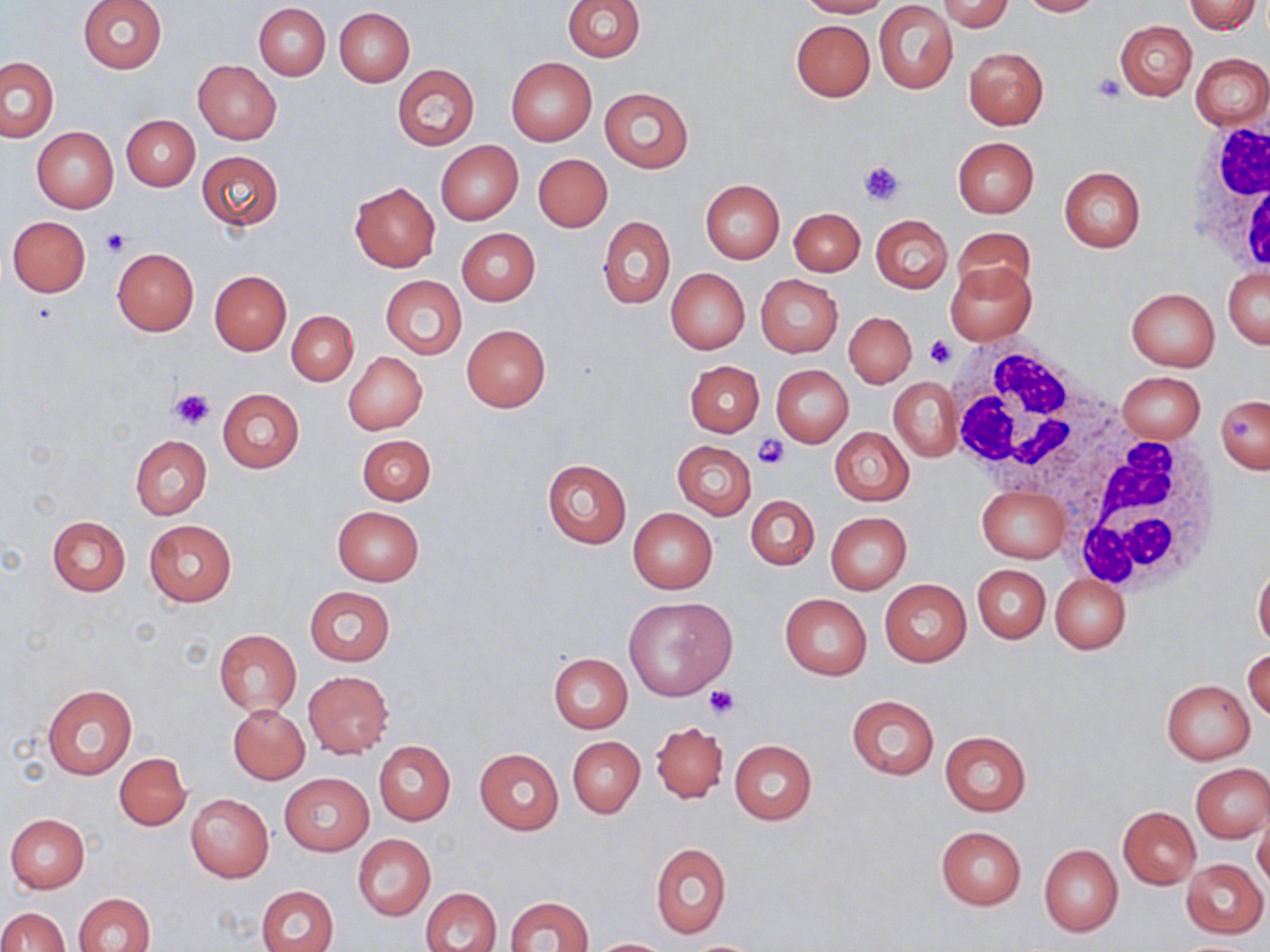
Summary:
  - Coordinate format: approximate bounding boxes as (x1,y1)-(x2,y2) corner pairs in pixels
  - White blood cell locations: (1182,115)-(1270,280), (940,343)-(1125,494), (1067,433)-(1222,595)
  - Uninfected red blood cell locations: (562,0)-(645,61), (797,0)-(891,18), (938,0)-(1013,31), (1017,0)-(1101,16), (1185,0)-(1260,34), (78,1)-(166,74), (254,3)-(330,80), (875,3)-(957,94), (335,8)-(415,87), (790,18)-(874,101), (1115,20)-(1196,101), (964,47)-(1047,129), (1190,53)-(1270,128), (0,57)-(58,142), (506,57)-(596,145), (193,59)-(281,143), (392,64)-(480,150), (600,88)-(693,172), (123,115)-(199,191), (32,127)-(119,213), (953,137)-(1039,218), (435,140)-(523,225), (196,150)-(283,230), (534,154)-(612,231), (1059,167)-(1145,253), (700,180)-(785,263), (349,181)-(440,271), (790,208)-(865,276), (870,214)-(952,292), (597,215)-(675,309), (8,216)-(91,296), (952,228)-(1036,304), (457,229)-(539,306), (111,248)-(199,335), (944,260)-(1037,346), (1224,267)-(1269,349), (665,268)-(749,354), (209,271)-(291,355), (755,275)-(842,356), (380,276)-(467,357), (1127,288)-(1219,370), (287,310)-(358,385), (844,312)-(915,387), (462,325)-(549,412), (344,352)-(427,435), (685,361)-(763,437), (771,365)-(853,447), (1117,371)-(1207,442), (889,376)-(962,462), (217,388)-(304,473), (1216,395)-(1270,474), (829,426)-(913,506), (357,434)-(436,505), (130,435)-(211,518), (672,441)-(756,518), (541,459)-(632,548), (977,485)-(1070,564), (745,496)-(819,570), (332,506)-(424,585), (628,507)-(717,594), (825,512)-(912,595), (47,515)-(130,597), (143,520)-(237,606), (1253,561)-(1270,648), (972,565)-(1050,642), (1050,575)-(1130,654), (879,579)-(971,666), (305,587)-(395,666), (780,594)-(872,679), (624,596)-(737,700), (214,629)-(301,716), (1244,648)-(1270,722), (548,653)-(632,733), (302,672)-(393,757), (1162,680)-(1254,763), (42,685)-(137,781), (846,694)-(939,780), (229,704)-(310,783), (651,721)-(727,803), (940,730)-(1031,816), (568,736)-(644,818), (730,739)-(817,825), (374,741)-(455,824), (475,749)-(564,833), (114,753)-(191,830), (1191,763)-(1270,842), (281,774)-(372,854), (186,794)-(273,882), (1118,806)-(1201,889), (1254,807)-(1270,890), (5,813)-(90,893), (935,825)-(1026,909), (352,834)-(435,920), (651,844)-(731,937), (1039,844)-(1123,936), (1180,859)-(1267,939), (258,885)-(339,952), (422,887)-(501,952), (73,892)-(155,952), (505,896)-(593,951), (0,907)-(68,952), (588,938)-(676,951)
  - Platelet locations: (1093,73)-(1128,102), (860,160)-(905,206), (101,229)-(130,256), (925,335)-(955,370), (171,389)-(214,430), (750,437)-(790,470), (705,686)-(739,718)
  - Slide-level diagnosis: negative for blood parasites
  - Field of view: one of a larger specimen
  - Magnification: 1000x
  - Modality: optical microscopy
  - Preparation: thin blood film
  - Stain: May-Grünwald-Giemsa
  - Image size: 1270×952 pixels